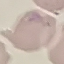

Summary:
  - Malaria status: uninfected
  - Image type: cell patch, automatically extracted from a larger field of view and resized to 64 × 64 pixels
  - Stain: Giemsa
  - Preparation: thin smear
  - Capture: smartphone through the microscope eyepiece